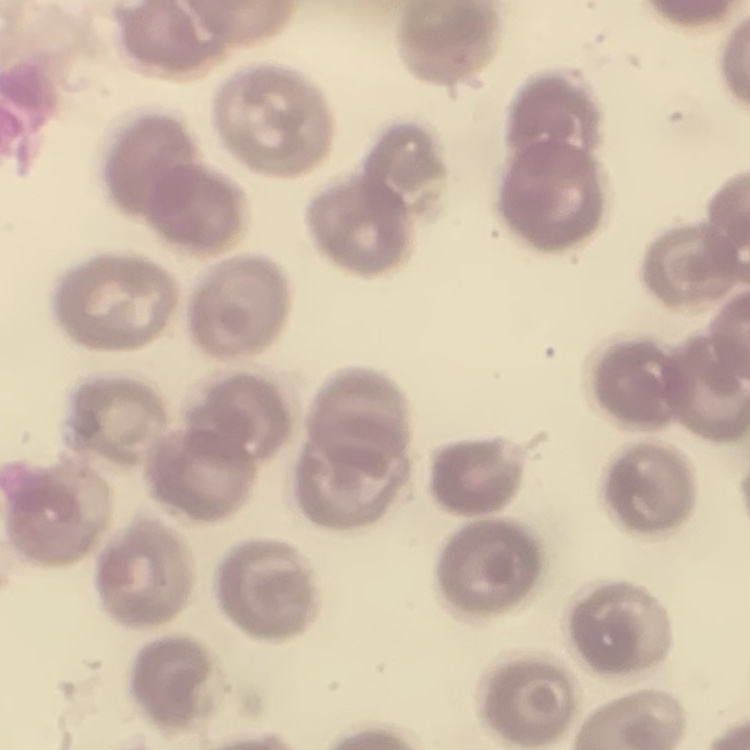
Summary:
  - Erythrocyte morphology: no rouleaux formation
  - Image type: one tile cut from a larger photomicrograph
  - Stain: Field's or Giemsa
  - Preparation: thin blood smear